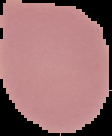 From a thin blood smear. Image is 112×136 pixels. The area outside the segmented cell region is set to black. Result: negative for malaria parasites.